Give the position of every Plasmodium parasite.
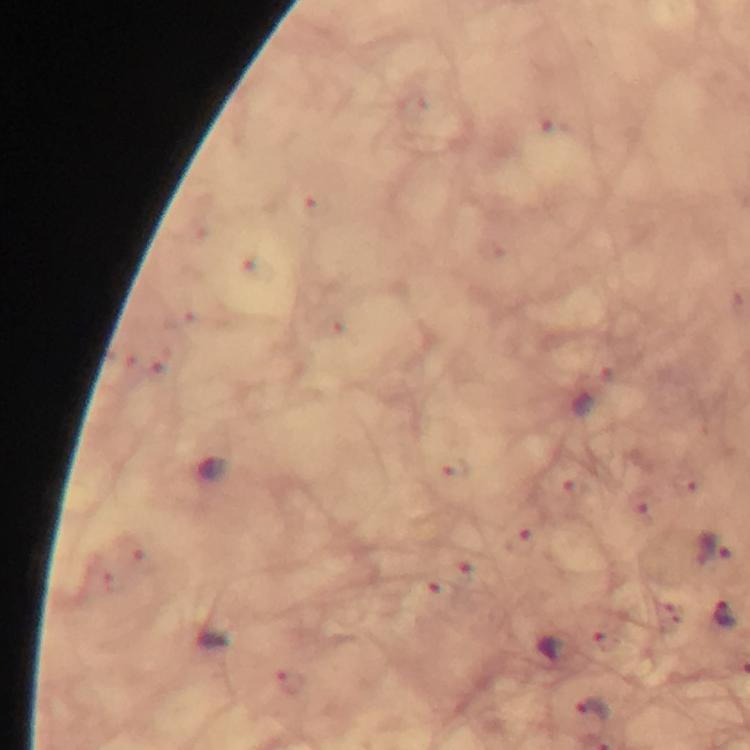
Approximate object centers, in pixels from the top-left corner.
Plasmodium parasites: (x=712, y=549), (x=727, y=613), (x=592, y=710).

Summary:
  - Stain: Giemsa
  - Cropped from: one field of view
  - Magnification: 100x
  - Image size: 750×750 pixels
  - Immersion oil: applied
  - Preparation: thick blood smear
  - Capture: smartphone photograph through a microscope
  - Context: from a diagnostic examination for malaria